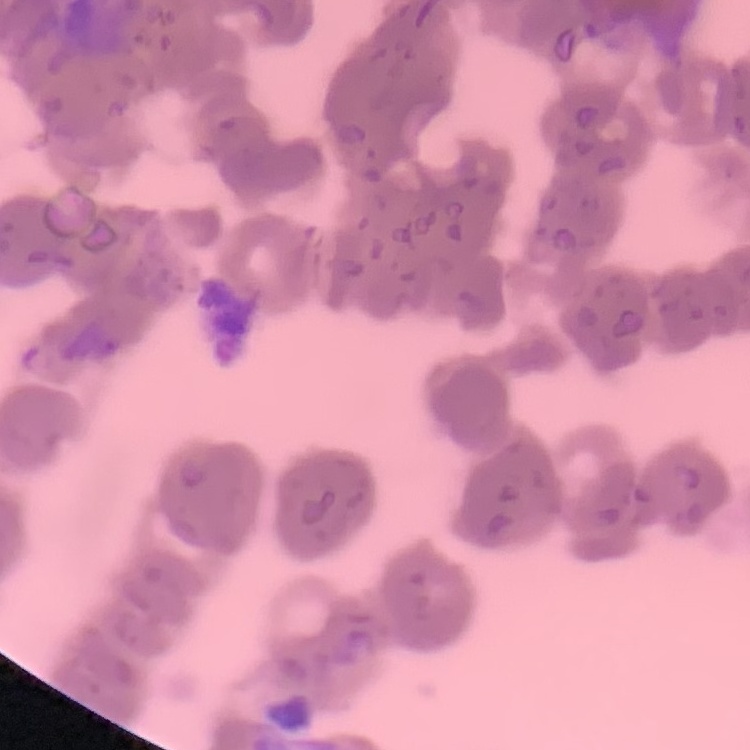
Summary:
  - Red blood cell morphology: rouleaux formation
  - Stain: Field's or Giemsa
  - Preparation: thin peripheral smear
  - Image type: square crop of a larger photomicrograph